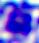 A leukocyte is shown. Captured at 400x magnification. Photomicrograph.